Identify the parasite.
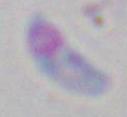
Toxoplasma gondii.

modality = photomicrograph
magnification = 1000x